Point out each Plasmodium parasite.
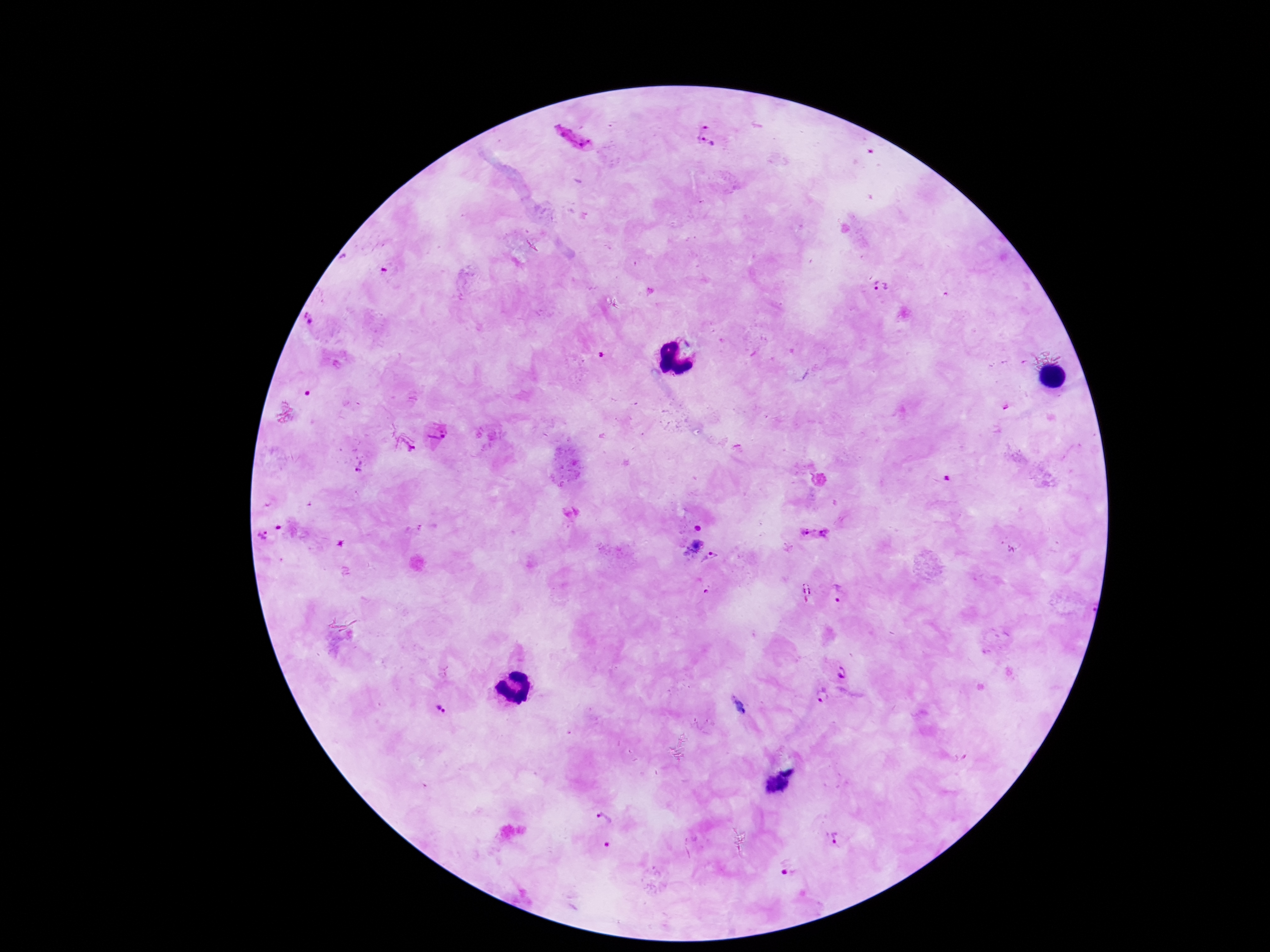

Approximate centers as {x, y} in pixels.
Plasmodium parasites: {706, 134}, {572, 138}, {882, 284}, {310, 320}, {1004, 407}, {437, 438}, {406, 444}, {359, 468}, {947, 478}, {281, 527}, {698, 527}, {807, 532}, {826, 534}, {261, 538}, {689, 543}, {711, 561}, {806, 591}, {705, 593}, {843, 593}, {842, 673}, {821, 697}, {440, 710}, {788, 764}, {774, 786}, {605, 819}, {838, 838}, {606, 847}, {786, 870}.

field of view = one from this slide
capture = smartphone camera through the microscope eyepiece
preparation = thick blood smear
image size = 1270×952 pixels
magnification = 100x
stain = Giemsa
patient malaria status = infected